Report the malaria status of this cell.
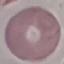

It is uninfected.

Summary:
  - Preparation: thin blood smear
  - Stain: Giemsa
  - Image type: cell patch, automatically extracted from a larger field of view and resized to 64 × 64 pixels
  - Capture: smartphone camera at the microscope eyepiece